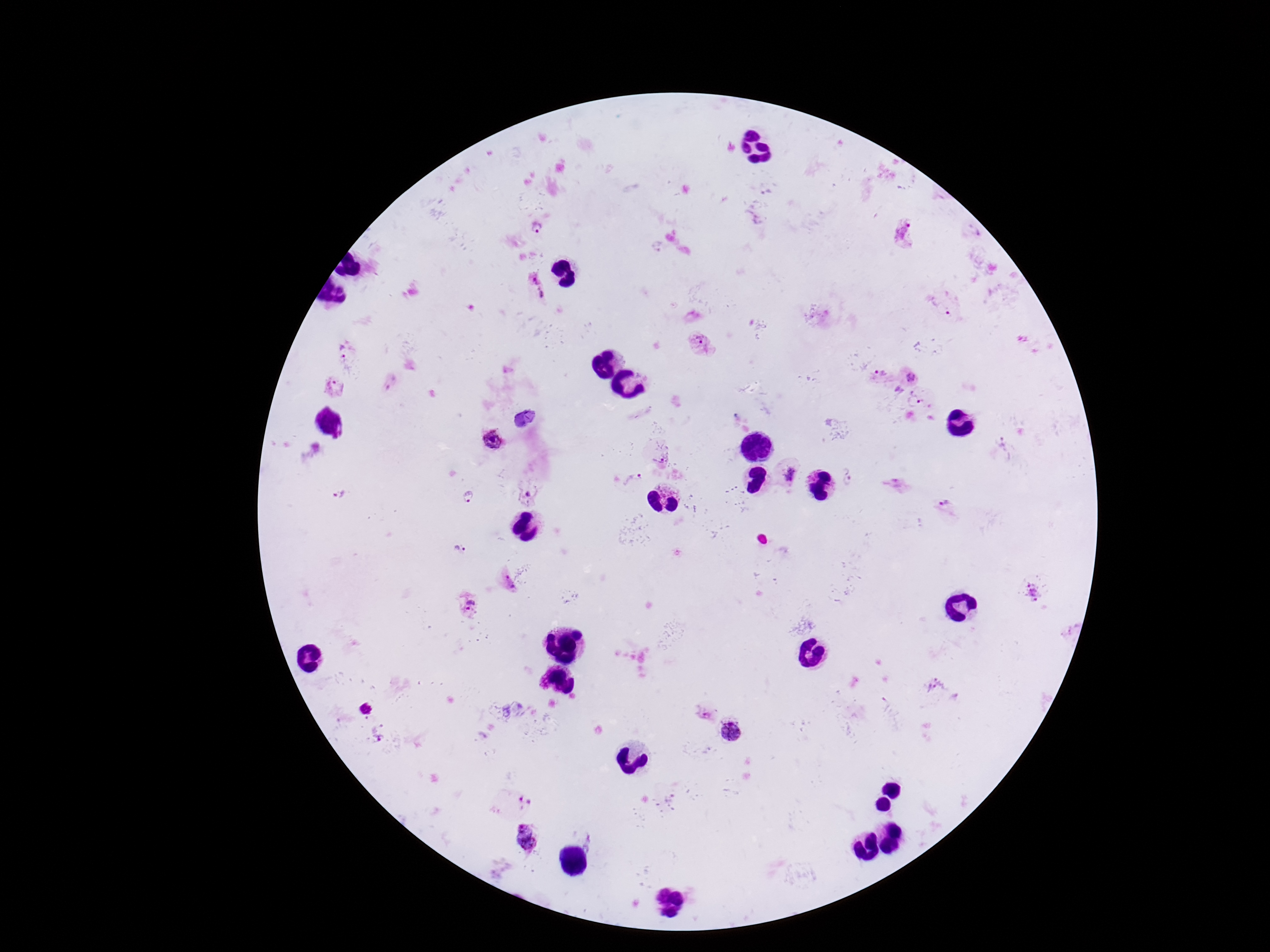

Approximate centers as [x, y] in pixels. Plasmodium parasite locations: [537, 227], [904, 233], [536, 289], [940, 308], [701, 343], [345, 351], [913, 374], [879, 375], [389, 381], [335, 387], [915, 401], [491, 439], [1008, 448], [663, 457], [787, 475], [846, 477], [635, 478], [895, 484], [530, 491], [341, 494], [468, 496], [946, 505], [459, 549], [507, 582], [1032, 593], [472, 603], [936, 688], [364, 708], [705, 712], [731, 732], [379, 738], [669, 798], [520, 803], [526, 836]. One field from this slide. 100x magnification. Image is 1270×952 pixels. Patient malaria status: positive. Thick blood smear. Giemsa-stained preparation. Photographed through the microscope eyepiece with a smartphone camera.